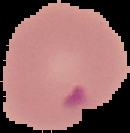
Malaria status: parasitized. Image is 130×133 pixels. From a thin blood smear. Segmented cell region on a black background.